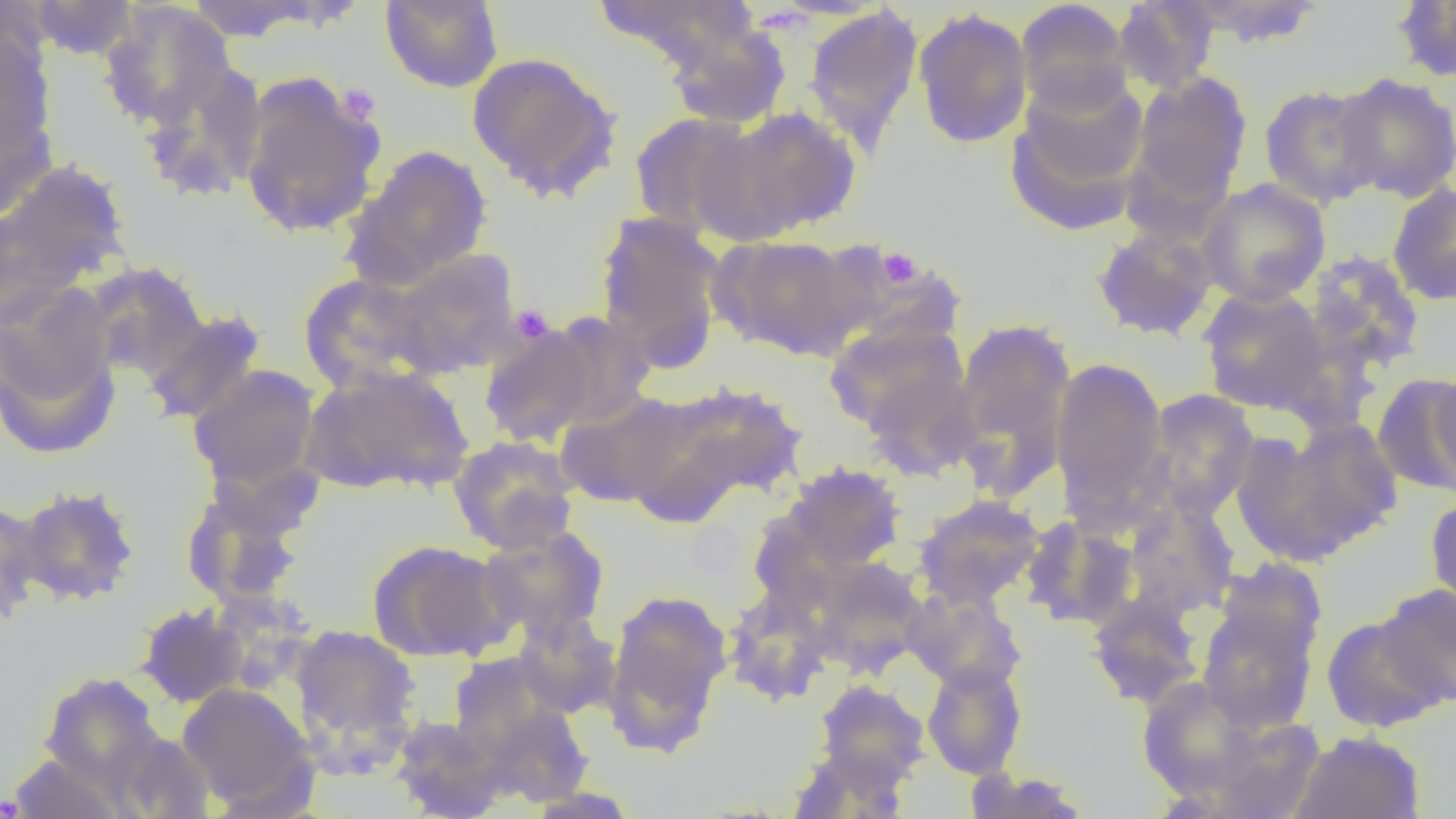

Summary:
  - Coordinate format: approximate bounding boxes as (x1,y1)-(x2,y2) corner pairs in pixels
  - Platelet locations: (335,83)-(381,126), (877,246)-(923,288), (509,304)-(555,343), (0,794)-(24,818)
  - Uninfected red blood cell locations: (179,0)-(335,42), (379,0)-(504,93), (594,0)-(755,74), (1178,0)-(1329,48), (26,1)-(141,61), (1015,1)-(1134,114), (1112,1)-(1220,95), (1389,1)-(1456,83), (98,2)-(236,131), (803,6)-(924,154), (913,7)-(1033,149), (659,14)-(793,131), (0,26)-(58,169), (466,51)-(623,203), (137,62)-(270,204), (238,72)-(385,240), (1129,72)-(1253,208), (1331,72)-(1455,203), (1005,76)-(1150,234), (1259,82)-(1384,209), (718,106)-(862,239), (628,111)-(765,239), (351,144)-(493,288), (0,158)-(131,302), (1196,179)-(1331,306), (1387,182)-(1456,306), (594,212)-(729,372), (1091,226)-(1218,341), (714,234)-(866,360), (386,249)-(524,377), (1304,250)-(1427,373), (83,260)-(210,383), (297,272)-(440,392), (1197,286)-(1330,414), (0,293)-(122,459), (142,308)-(267,425), (542,313)-(656,431), (949,317)-(1077,497), (824,319)-(970,439), (478,324)-(600,448), (1050,358)-(1169,516), (188,364)-(321,492), (1426,364)-(1455,498), (300,365)-(475,497), (1374,373)-(1456,498), (652,381)-(808,506), (1141,389)-(1260,519), (557,391)-(689,508), (1234,420)-(1401,563), (448,435)-(580,554), (779,463)-(907,573), (181,480)-(312,608), (14,485)-(140,606), (914,494)-(1046,608), (1424,494)-(1456,615), (0,498)-(43,627), (1123,499)-(1240,618), (1021,517)-(1137,629), (477,524)-(609,641), (367,539)-(512,663), (813,558)-(928,678), (1378,583)-(1456,707), (602,587)-(733,753), (724,589)-(833,705), (904,589)-(1027,695), (1086,590)-(1205,709), (1197,598)-(1321,734), (135,602)-(250,708), (511,611)-(620,718), (1321,614)-(1447,733), (290,625)-(421,755), (450,654)-(571,760), (921,661)-(1027,779), (38,672)-(164,791), (1136,676)-(1271,802), (813,679)-(929,788), (177,683)-(315,813), (473,697)-(593,807), (389,715)-(506,819), (1193,715)-(1325,819), (104,729)-(215,818), (1289,731)-(1426,819), (790,744)-(906,819), (8,751)-(129,819), (962,767)-(1091,818), (522,787)-(641,818)
  - Slide-level diagnosis: no evidence of blood parasites
  - Modality: light microscopy
  - Magnification: 1000x
  - Preparation: thin blood film
  - Field of view: one of a larger specimen
  - Image size: 1456×819 pixels